Locate every uninfected red blood cell.
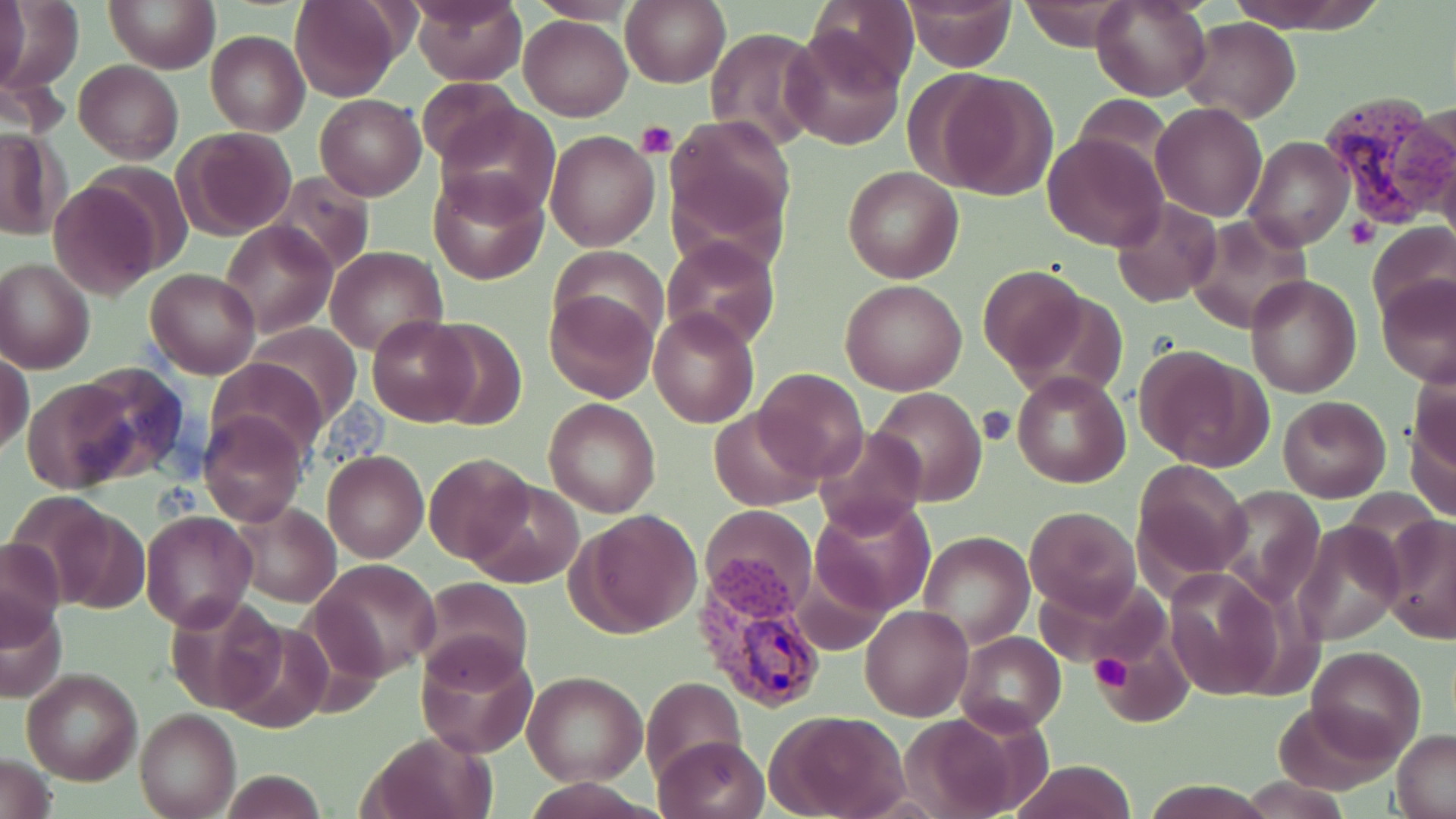

Approximate bounding boxes as [x1, y1, x2, y2] in pixels.
Uninfected red blood cells: [95, 0, 210, 147], [103, 0, 219, 73], [290, 0, 400, 102], [411, 0, 527, 85], [526, 0, 647, 24], [806, 0, 918, 91], [898, 0, 1017, 71], [1091, 0, 1213, 103], [1224, 0, 1383, 33], [0, 1, 85, 94], [2, 1, 29, 92], [1018, 1, 1134, 52], [621, 2, 729, 87], [520, 16, 633, 120], [1180, 17, 1299, 123], [705, 27, 825, 154], [781, 27, 905, 150], [205, 30, 309, 137], [74, 60, 184, 164], [923, 68, 1058, 199], [416, 77, 523, 167], [314, 94, 426, 200], [1071, 95, 1172, 178], [1151, 102, 1268, 221], [436, 106, 560, 221], [666, 115, 796, 249], [0, 127, 65, 240], [176, 128, 296, 241], [544, 130, 660, 251], [1042, 132, 1167, 253], [1244, 135, 1354, 253], [842, 164, 964, 283], [429, 169, 547, 284], [266, 172, 376, 279], [48, 176, 164, 295], [1110, 197, 1222, 307], [1185, 216, 1312, 333], [218, 220, 338, 338], [1368, 221, 1456, 325], [1215, 230, 1344, 368], [660, 235, 780, 350], [324, 245, 449, 356], [551, 246, 669, 344], [0, 256, 95, 374], [977, 265, 1087, 376], [146, 268, 262, 379], [1245, 275, 1363, 398], [1377, 276, 1455, 388], [840, 279, 968, 396], [544, 288, 660, 403], [649, 309, 758, 428], [368, 315, 480, 425], [421, 318, 529, 430], [238, 325, 364, 429], [1135, 344, 1270, 472], [1, 349, 34, 457], [208, 358, 328, 462], [68, 364, 193, 480], [753, 368, 869, 483], [1011, 370, 1131, 489], [22, 375, 143, 492], [870, 387, 986, 506], [1277, 396, 1391, 503], [543, 397, 662, 518], [1408, 398, 1456, 522], [710, 406, 823, 511], [198, 409, 307, 527], [815, 425, 927, 536], [323, 451, 428, 561], [422, 451, 537, 565], [1132, 460, 1254, 585], [465, 480, 585, 588], [1213, 485, 1326, 607], [811, 496, 935, 616], [39, 501, 149, 615], [228, 501, 343, 607], [701, 506, 817, 617], [1025, 506, 1141, 618], [140, 510, 257, 631], [572, 510, 702, 636], [1381, 516, 1456, 644], [1294, 520, 1402, 645], [918, 533, 1034, 646], [0, 538, 66, 647], [311, 557, 440, 679], [1164, 569, 1283, 701], [1032, 573, 1168, 670], [416, 578, 533, 687], [165, 594, 287, 715], [1, 598, 69, 703], [860, 604, 973, 721], [220, 612, 334, 731], [1100, 631, 1190, 725], [956, 632, 1066, 734], [417, 643, 537, 759], [1307, 646, 1425, 759], [21, 669, 142, 785], [524, 673, 646, 785], [641, 677, 746, 783], [1274, 701, 1397, 795], [135, 710, 239, 819], [769, 711, 911, 819], [898, 711, 1028, 816], [359, 731, 495, 819], [1392, 731, 1456, 818], [654, 736, 769, 819], [0, 754, 56, 818], [1010, 759, 1135, 819], [219, 770, 330, 818], [1238, 778, 1355, 817].

Platelet locations: [637, 121, 677, 160], [1348, 217, 1378, 248], [977, 404, 1017, 447], [1090, 655, 1132, 691]. Plasmodium vivax-infected red blood cell locations: [1322, 93, 1449, 232], [697, 572, 832, 713]. Slide-level diagnosis: Plasmodium vivax. Image is 1456×819 pixels. Optical microscopy. 1000x magnification. May-Grünwald-Giemsa-stained preparation. One field of a larger specimen. Thin blood smear.